Identify the cell.
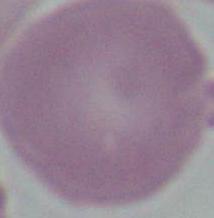

This is an erythrocyte.

modality: micrograph
magnification: 1000x